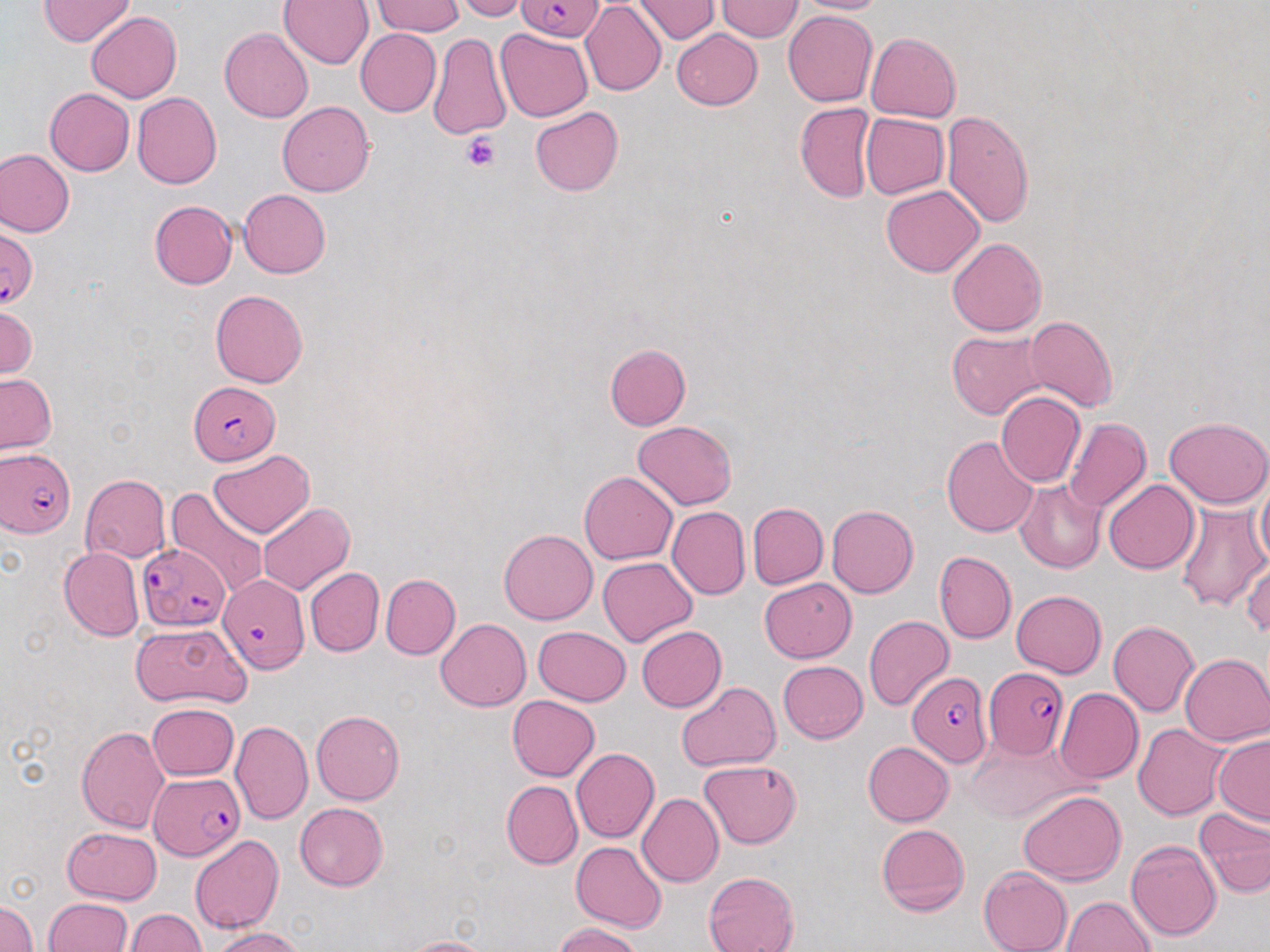

Plasmodium falciparum-infected red blood cell locations = approximate bounding boxes as (x1, y1, x2, y2) in pixels: (517, 0, 603, 42), (0, 227, 38, 309), (190, 380, 280, 464), (1, 447, 75, 537), (137, 543, 228, 631), (219, 571, 308, 673), (983, 669, 1069, 758), (907, 671, 991, 766), (149, 772, 245, 860)
slide-level diagnosis = Plasmodium falciparum
modality = optical microscopy
platelet locations = approximate bounding boxes as (x1, y1, x2, y2) in pixels: (461, 132, 500, 173)
uninfected red blood cell locations = approximate bounding boxes as (x1, y1, x2, y2) in pixels: (39, 0, 133, 46), (455, 0, 531, 22), (792, 0, 892, 14), (280, 1, 373, 70), (372, 1, 465, 37), (580, 1, 666, 97), (632, 1, 720, 43), (718, 1, 802, 42), (783, 11, 877, 107), (87, 12, 181, 103), (220, 28, 313, 123), (496, 28, 592, 121), (671, 28, 763, 109), (355, 29, 442, 117), (866, 32, 961, 122), (428, 33, 512, 139), (45, 88, 135, 176), (133, 91, 222, 189), (277, 101, 375, 196), (795, 102, 875, 203), (530, 106, 624, 195), (942, 110, 1035, 227), (860, 112, 950, 199), (0, 149, 74, 238), (881, 184, 983, 277), (239, 189, 331, 278), (149, 200, 237, 289), (945, 237, 1047, 336), (210, 289, 307, 387), (1, 304, 38, 382), (1025, 315, 1118, 412), (947, 331, 1049, 420), (604, 344, 690, 430), (0, 374, 56, 454), (995, 392, 1086, 487), (1164, 416, 1270, 508), (1063, 418, 1151, 512), (632, 421, 739, 510), (942, 435, 1038, 537), (209, 450, 315, 538), (1255, 469, 1270, 574), (579, 471, 677, 565), (79, 475, 170, 562), (1013, 479, 1106, 573), (1103, 479, 1198, 574), (167, 487, 269, 596), (747, 502, 828, 589), (1176, 502, 1269, 612), (258, 503, 354, 595), (827, 504, 919, 598), (666, 506, 750, 600), (499, 529, 598, 624), (59, 546, 145, 642), (933, 551, 1016, 644), (598, 557, 696, 646), (1243, 558, 1270, 637), (305, 567, 384, 657), (381, 574, 460, 659), (760, 578, 856, 662), (1012, 590, 1106, 677), (864, 615, 954, 711), (435, 618, 531, 711), (1108, 621, 1200, 717), (132, 622, 251, 707), (636, 625, 727, 711), (533, 626, 631, 705), (1180, 653, 1270, 746), (778, 660, 868, 743), (674, 681, 781, 772), (1055, 687, 1143, 784), (507, 695, 599, 780), (148, 702, 239, 781), (311, 710, 405, 805), (230, 719, 314, 826), (1133, 724, 1229, 820), (75, 725, 169, 833), (1213, 734, 1270, 827), (967, 735, 1080, 819), (862, 741, 954, 826), (571, 748, 660, 844), (699, 759, 802, 849), (501, 781, 581, 867), (1019, 789, 1127, 884), (636, 793, 723, 887), (295, 802, 388, 890), (1195, 808, 1270, 897), (875, 823, 970, 917), (62, 826, 162, 903), (190, 835, 283, 934), (572, 841, 666, 931), (1126, 841, 1221, 941), (978, 866, 1072, 952), (1074, 868, 1212, 947), (702, 872, 800, 952), (1061, 896, 1154, 951), (0, 897, 38, 952), (44, 898, 134, 951), (123, 908, 207, 951), (553, 922, 646, 952), (211, 926, 307, 952), (401, 936, 496, 952)
image size = 1270×952 pixels
stain = May-Grünwald-Giemsa
preparation = thin blood film
field of view = one of a larger specimen
magnification = 1000x